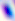
Summary:
  - Identification: Toxoplasma gondii
  - Magnification: 400x
  - Modality: photomicrograph